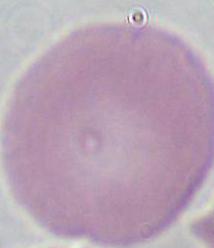

Summary:
  - Modality: photomicrograph
  - Identification: erythrocyte
  - Magnification: 1000x